Assess this cell for malaria.
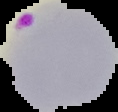

It is parasitized.

Summary:
  - Image size: 118×112 pixels
  - Image type: segmented cell region with the area outside set to black
  - Preparation: thin blood film